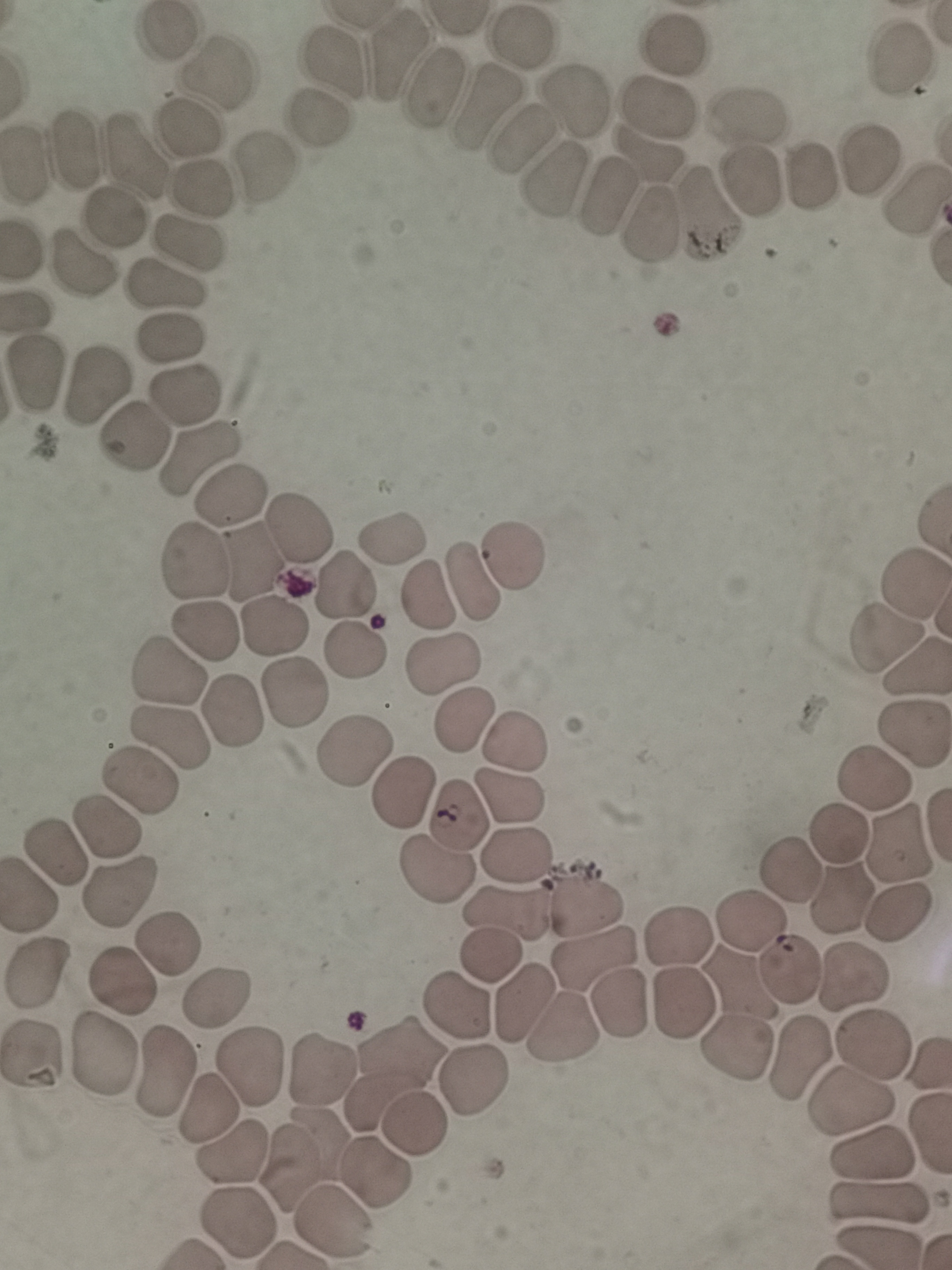 Approximate object centers, in pixels from the top-left corner. Cell locations: (x=166, y=34), (x=521, y=39), (x=674, y=45), (x=396, y=51), (x=896, y=58), (x=330, y=61), (x=218, y=76), (x=433, y=86), (x=485, y=103), (x=577, y=103), (x=658, y=107), (x=747, y=115), (x=317, y=123), (x=190, y=127), (x=517, y=137), (x=78, y=147), (x=649, y=155), (x=137, y=158), (x=867, y=160), (x=27, y=163), (x=261, y=174), (x=811, y=174), (x=549, y=178), (x=751, y=179), (x=202, y=191), (x=605, y=191), (x=915, y=197), (x=709, y=213), (x=115, y=220), (x=648, y=223), (x=187, y=245), (x=84, y=263), (x=168, y=286), (x=171, y=340), (x=33, y=367), (x=93, y=383), (x=186, y=393), (x=133, y=438), (x=199, y=461), (x=228, y=499), (x=300, y=525), (x=392, y=540), (x=509, y=558), (x=255, y=560), (x=194, y=564), (x=473, y=583), (x=344, y=585), (x=914, y=587), (x=430, y=596), (x=275, y=626), (x=205, y=632), (x=887, y=641), (x=352, y=648), (x=442, y=664), (x=914, y=671), (x=166, y=674), (x=294, y=693), (x=231, y=717), (x=465, y=720), (x=911, y=734), (x=171, y=736), (x=511, y=742), (x=353, y=747), (x=871, y=777), (x=141, y=778), (x=400, y=789), (x=510, y=797), (x=456, y=816), (x=111, y=825), (x=837, y=835), (x=897, y=842), (x=516, y=853), (x=57, y=854), (x=789, y=870), (x=437, y=874), (x=118, y=886), (x=841, y=896), (x=588, y=902), (x=897, y=912), (x=502, y=915), (x=749, y=921), (x=679, y=938), (x=166, y=941), (x=487, y=955), (x=591, y=956), (x=37, y=971), (x=790, y=971), (x=849, y=977), (x=123, y=981), (x=737, y=988), (x=216, y=994), (x=525, y=1002), (x=622, y=1002), (x=681, y=1002), (x=453, y=1004), (x=563, y=1025), (x=871, y=1043), (x=736, y=1050), (x=100, y=1055), (x=802, y=1057), (x=31, y=1058), (x=248, y=1067), (x=163, y=1071), (x=321, y=1071), (x=396, y=1071), (x=477, y=1083), (x=850, y=1100), (x=209, y=1111), (x=414, y=1131), (x=870, y=1150), (x=228, y=1154), (x=303, y=1156), (x=377, y=1173), (x=877, y=1199), (x=237, y=1221), (x=335, y=1221). One field from this slide. Photographed with a smartphone camera at the microscope eyepiece. Giemsa stain. Image is 952×1270 pixels. Thin blood film.